Classify this cell by malaria status.
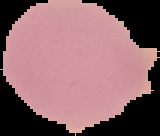
It is uninfected.

Summary:
  - Image size: 160×136 pixels
  - Image type: segmented cell region with the area outside set to black
  - Preparation: thin blood smear